Classify this cell by malaria status.
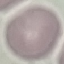
It is uninfected.

stain = Giemsa
preparation = thin smear
capture = smartphone through the microscope eyepiece
image type = automatically extracted cell patch, resized to 64 × 64 pixels